Give the position of every Plasmodium parasite.
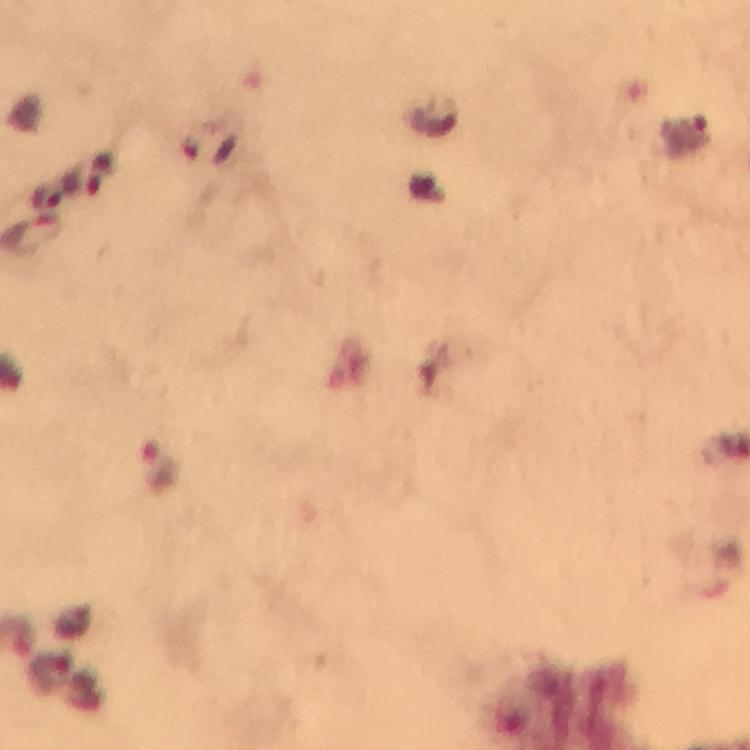

Approximate object centers, in pixels from the top-left corner.
Plasmodium parasites: (x=688, y=132), (x=207, y=147), (x=103, y=174), (x=48, y=195), (x=158, y=468).

preparation = thick smear
immersion oil = applied
cropped from = a single field of view
image size = 750×750 pixels
stain = Giemsa
context = from a malaria diagnostic workup
magnification = 100x
capture = smartphone camera through the microscope